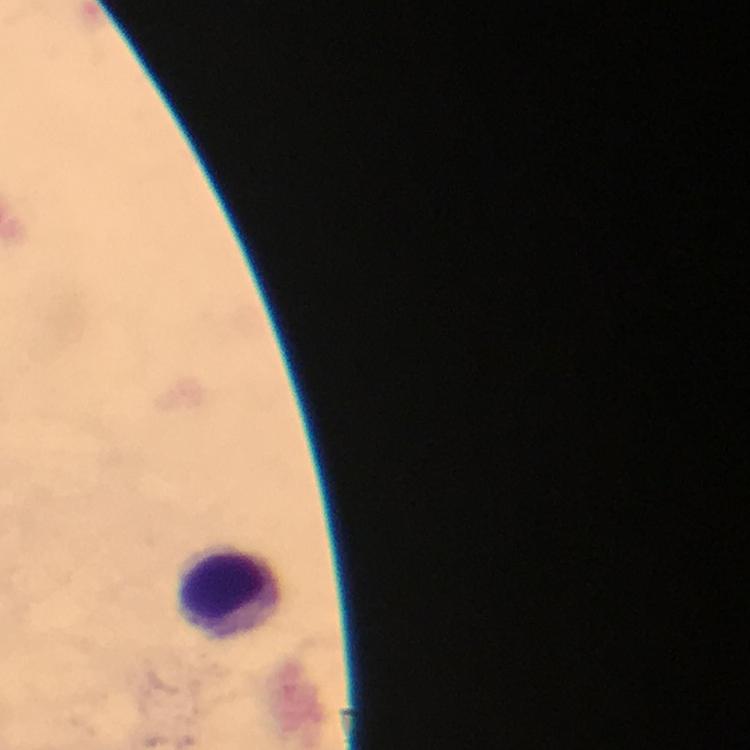 Approximate centers as {x, y} in pixels. Leukocyte locations: {236, 590}. Photographed through the microscope with a smartphone camera. Malaria parasites: none detected. At 100x magnification. From a malaria diagnostic workup. Immersion oil applied. Thick smear. Giemsa-stained preparation. Image is 750×750 pixels. Cropped region of a single field of view.